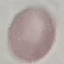
Summary:
  - Malaria status: uninfected
  - Stain: Giemsa
  - Capture: smartphone camera at the microscope eyepiece
  - Image type: automatically extracted cell patch, resized to 64 × 64 pixels
  - Preparation: thin blood film